Report the malaria status of this cell.
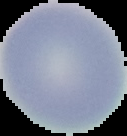
Uninfected.

Summary:
  - Image type: cell region segmented out of the field of view; surrounding area masked to black
  - Image size: 127×136 pixels
  - Preparation: thin blood film